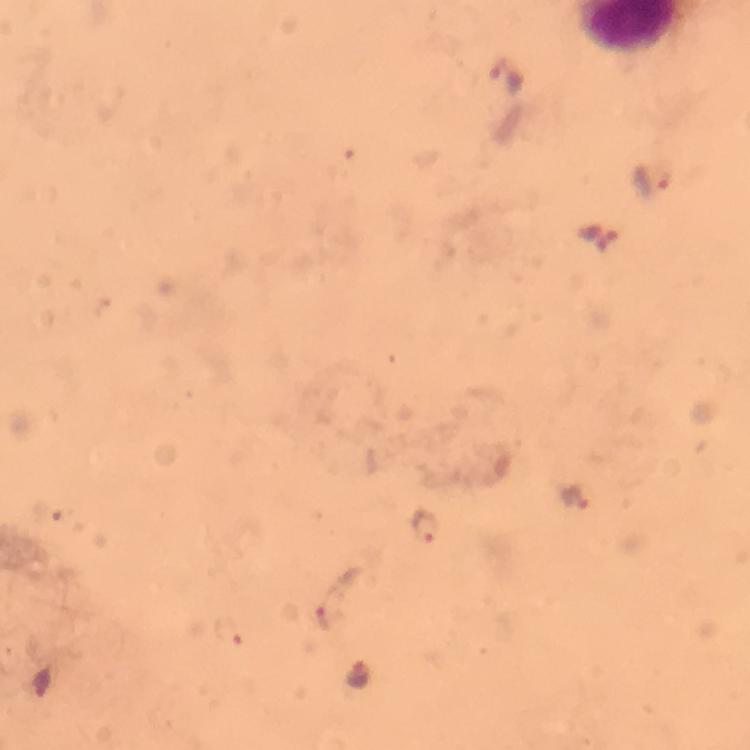
Approximate centers as [x, y] in pixels. Plasmodium parasite locations: [506, 74], [651, 179], [576, 496], [424, 530], [327, 617], [229, 631], [361, 677]. Thick smear. From a diagnostic examination for malaria. Image is 750×750 pixels. A crop from one field of view. Giemsa stain. Immersion oil was used. Photographed through the microscope with a smartphone camera. At 100x magnification.